Assess this cell for malaria.
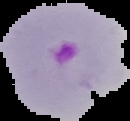

It is parasitized.

Summary:
  - Image size: 130×121 pixels
  - Preparation: thin blood smear
  - Image type: cell region segmented out of the field of view; surrounding area masked to black